Locate every Plasmodium parasite.
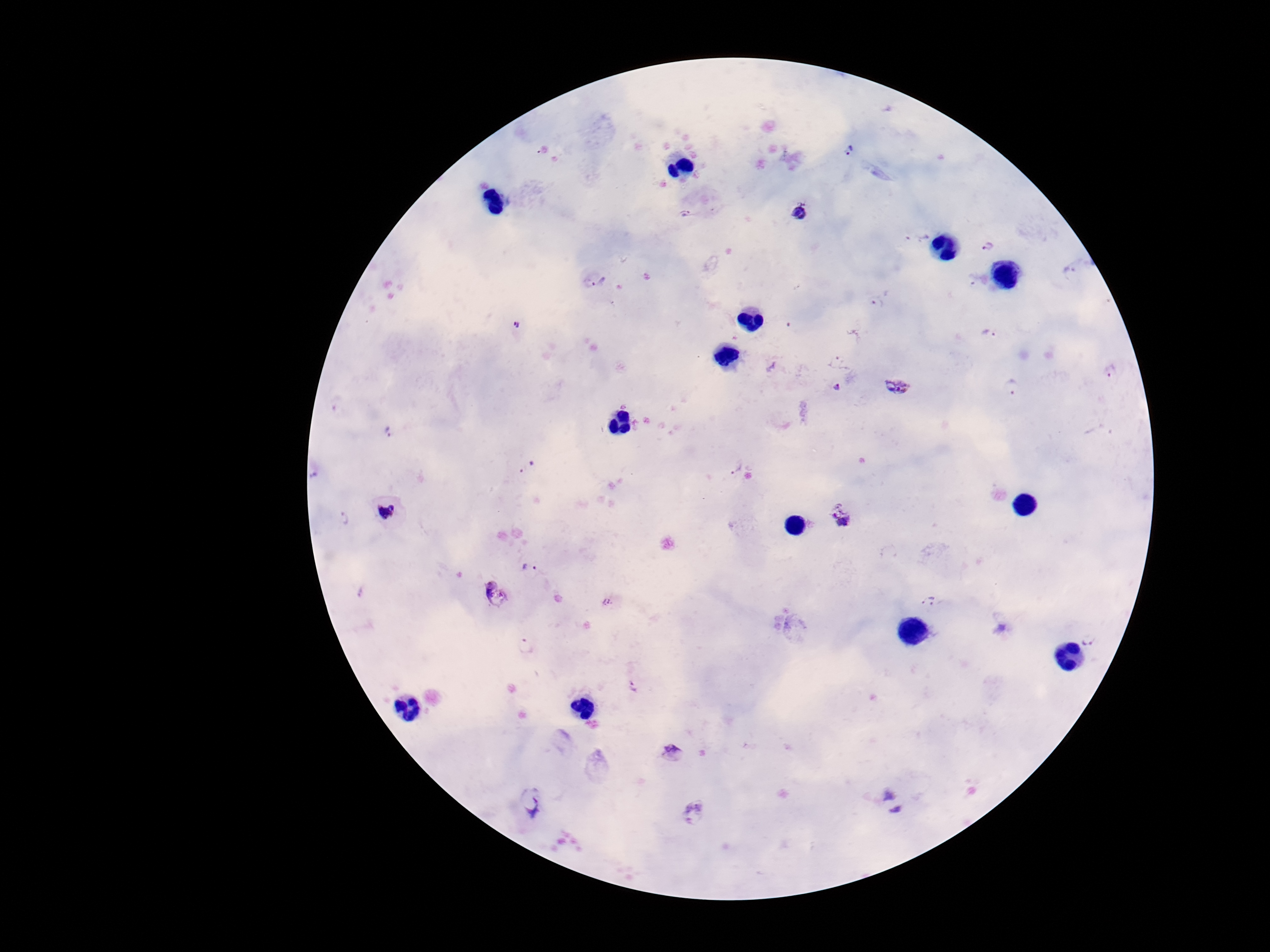

Approximate object centers, in pixels from the top-left corner.
Plasmodium parasites: (x=849, y=149), (x=799, y=212), (x=686, y=213), (x=918, y=237), (x=987, y=246), (x=1071, y=273), (x=595, y=278), (x=878, y=303), (x=518, y=326), (x=990, y=333), (x=839, y=360), (x=1010, y=385), (x=897, y=386), (x=837, y=387), (x=389, y=434), (x=735, y=466), (x=528, y=468), (x=388, y=513), (x=842, y=515), (x=345, y=517), (x=529, y=570), (x=495, y=592), (x=930, y=602), (x=612, y=603), (x=1091, y=637), (x=526, y=645), (x=634, y=686), (x=672, y=751), (x=889, y=792), (x=533, y=802), (x=897, y=811), (x=692, y=813).

{
  "field_of_view": "one from this slide",
  "capture": "smartphone camera through the microscope eyepiece",
  "patient_malaria_status": "infected",
  "magnification": "100x",
  "stain": "Giemsa",
  "preparation": "thick blood film",
  "image_size": "1270×952 pixels"
}